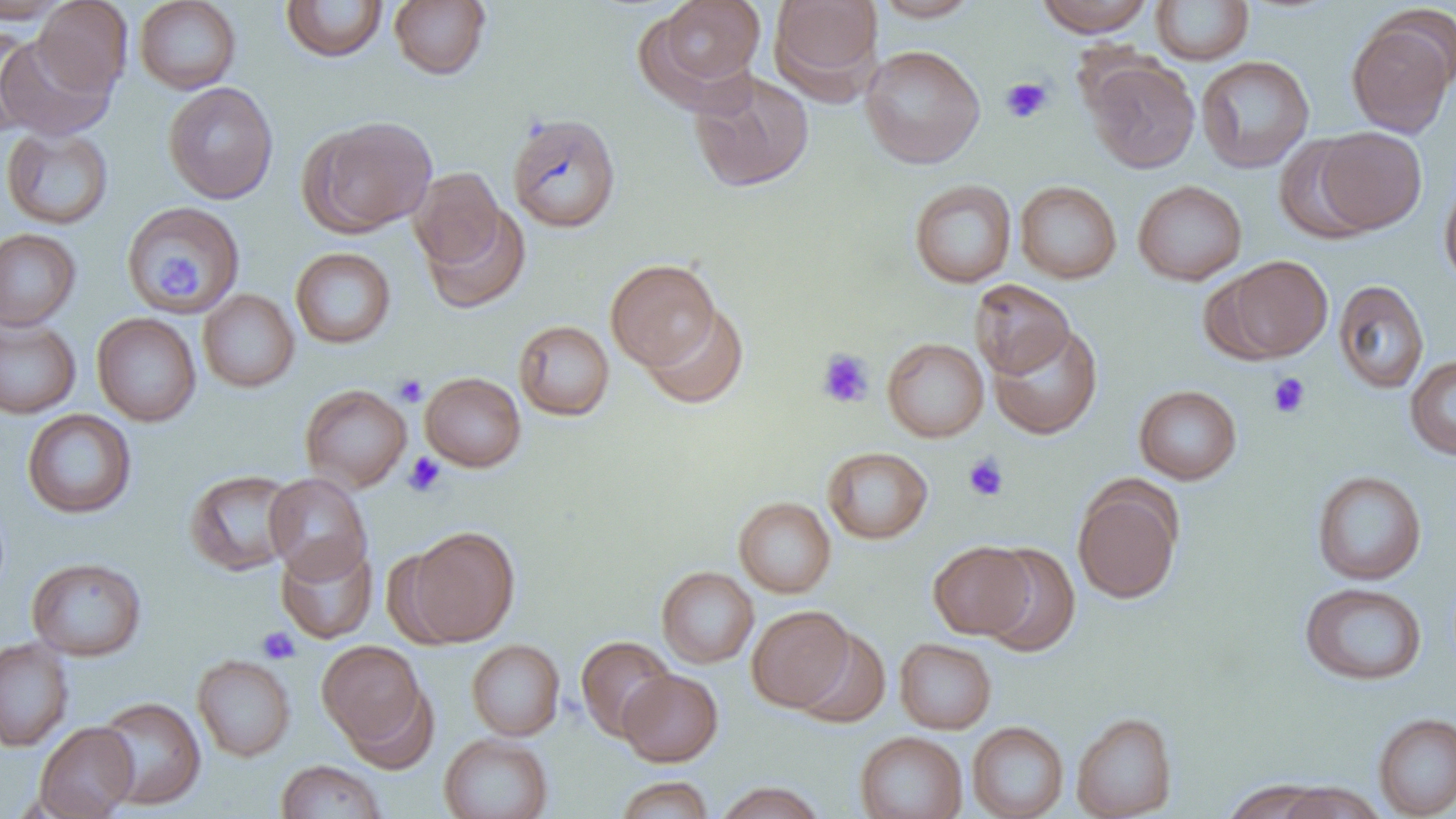

Approximate bounding boxes as (x1,y1)-(x2,y2) corner pairs in pixels. Platelet locations: (1001,77)-(1053,124), (159,256)-(197,298), (816,349)-(875,409), (1267,372)-(1311,418), (393,374)-(428,407), (403,452)-(446,497), (963,453)-(1009,501), (256,626)-(300,664). Uninfected red blood cell locations: (0,0)-(71,24), (33,0)-(132,97), (134,0)-(241,94), (389,0)-(492,80), (651,0)-(767,92), (769,0)-(883,97), (872,0)-(982,22), (1036,0)-(1154,37), (1151,0)-(1254,65), (280,1)-(388,62), (1345,15)-(1455,138), (0,25)-(41,135), (0,34)-(116,141), (860,44)-(985,169), (1196,55)-(1314,173), (1084,57)-(1200,173), (689,69)-(814,192), (163,82)-(278,204), (507,112)-(622,234), (303,116)-(436,236), (1,126)-(114,230), (1313,127)-(1427,235), (1274,135)-(1379,244), (410,167)-(504,268), (1439,178)-(1456,290), (909,179)-(1017,288), (1015,180)-(1122,283), (1133,180)-(1247,285), (120,202)-(246,315), (421,204)-(531,313), (0,228)-(82,331), (290,247)-(396,348), (1214,256)-(1333,362), (605,258)-(720,371), (969,279)-(1075,379), (1333,279)-(1429,393), (198,289)-(300,392), (642,304)-(749,409), (92,313)-(201,426), (0,317)-(81,418), (513,320)-(615,421), (988,324)-(1103,439), (882,337)-(989,443), (1405,355)-(1456,460), (420,372)-(526,472), (300,384)-(412,492), (1133,384)-(1242,485), (21,409)-(137,518), (822,446)-(933,544), (185,469)-(300,577), (1312,470)-(1427,585), (264,473)-(372,583), (1072,480)-(1184,604), (734,497)-(836,598), (404,526)-(520,646), (277,539)-(377,644), (928,541)-(1034,639), (978,543)-(1081,658), (26,557)-(147,661), (657,566)-(759,668), (1299,581)-(1427,685), (747,605)-(853,711), (790,627)-(891,729), (575,635)-(676,741), (0,637)-(74,751), (895,638)-(996,734), (466,639)-(565,741), (317,641)-(428,750), (192,654)-(296,762), (618,669)-(723,767), (343,682)-(438,773), (94,696)-(206,810), (1071,712)-(1177,819), (1373,712)-(1456,818), (34,721)-(138,819), (967,721)-(1069,819), (855,730)-(968,819), (439,733)-(554,819), (275,760)-(387,818), (615,776)-(714,818), (1222,778)-(1330,819), (714,781)-(826,818), (1276,782)-(1386,819). Slide-level diagnosis: negative for blood parasites. Thin blood film. Image is 1456×819 pixels. Optical microscopy. Single field of view. Captured at 1000x magnification.